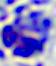
{
  "identification": "white blood cell",
  "modality": "photomicrograph",
  "magnification": "400x"
}